Describe the morphology of the erythrocytes.
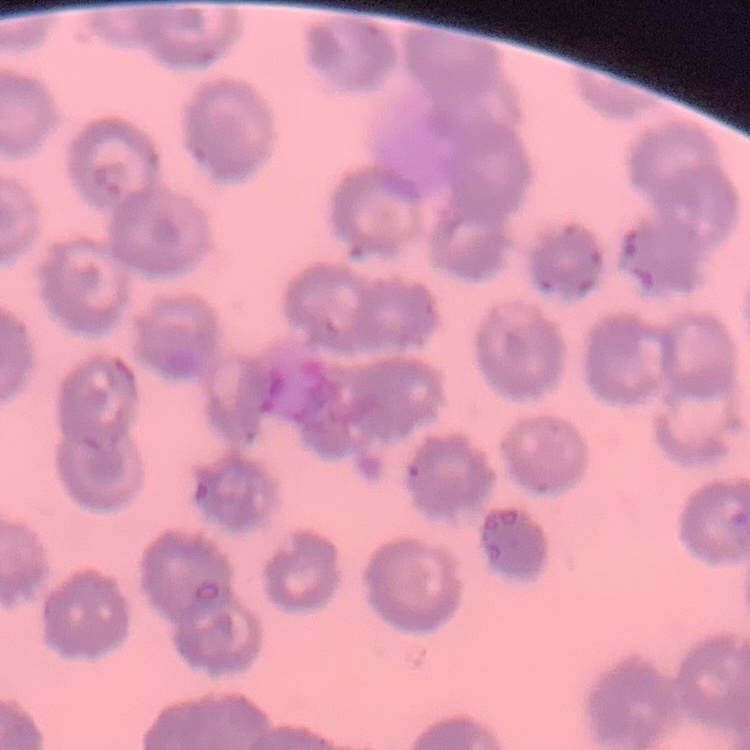
No rouleaux formation.

Summary:
  - Image type: one tile cut from a larger photomicrograph
  - Stain: Field's or Giemsa
  - Preparation: thin blood film